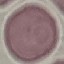

result = negative for malaria parasites
capture = smartphone camera at the microscope eyepiece
preparation = thin blood smear
stain = Giemsa
image type = cell patch, automatically extracted from a larger field of view and resized to 64 × 64 pixels